Give the extent of all Plasmodium malariae-infected red blood cells.
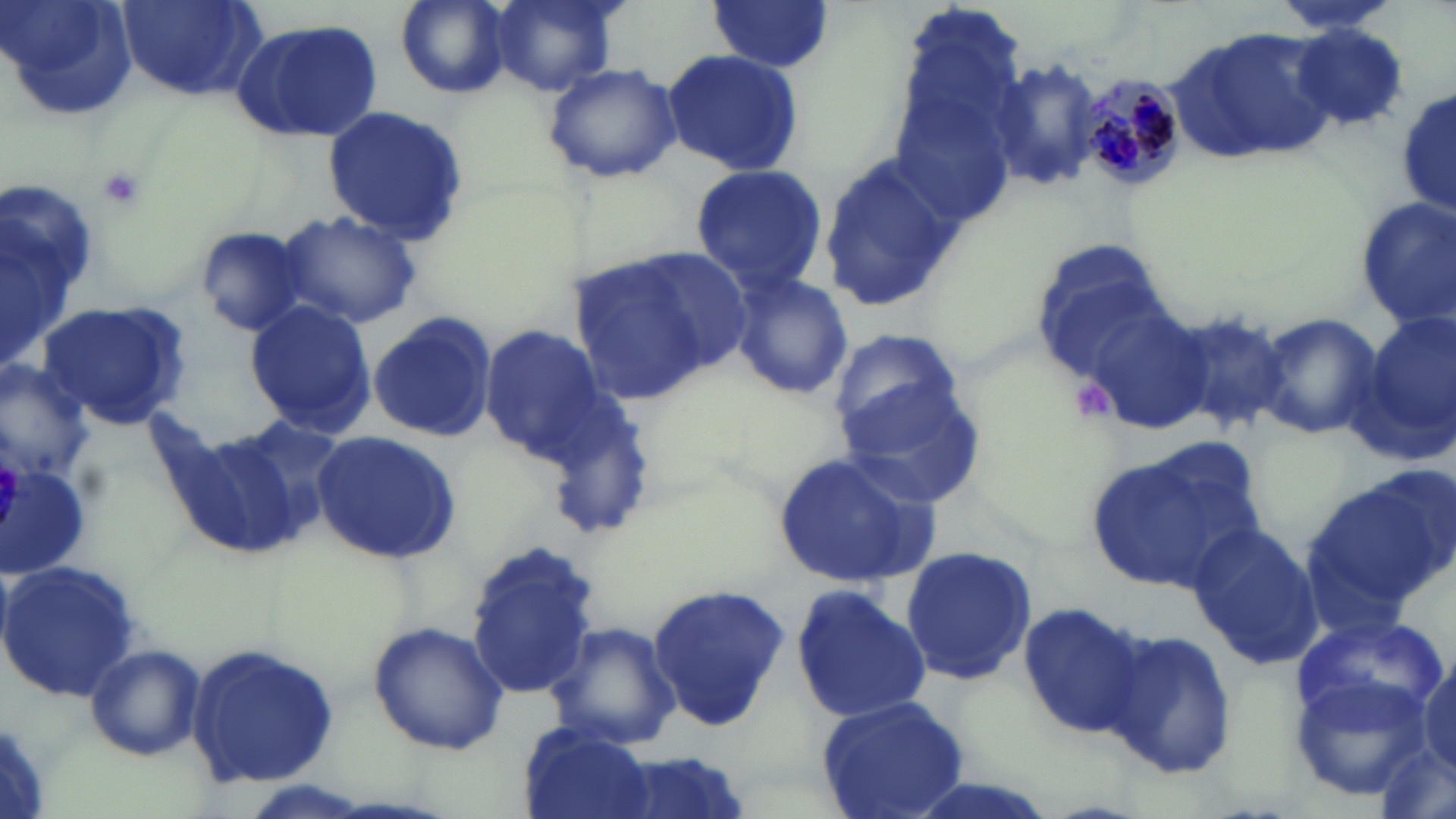

Approximate bounding boxes as named x1/y1/x2/y2 corners in pixels.
Plasmodium malariae-infected red blood cells: (x1=1078, y1=76, x2=1185, y2=193).

slide-level diagnosis = Plasmodium malariae
platelet locations = approximate bounding boxes as named x1/y1/x2/y2 corners in pixels: (x1=93, y1=166, x2=147, y2=210), (x1=1070, y1=381, x2=1116, y2=420)
uninfected red blood cell locations = approximate bounding boxes as named x1/y1/x2/y2 corners in pixels: (x1=1, y1=0, x2=138, y2=123), (x1=118, y1=0, x2=265, y2=103), (x1=394, y1=0, x2=511, y2=98), (x1=489, y1=0, x2=620, y2=95), (x1=705, y1=1, x2=837, y2=75), (x1=1271, y1=2, x2=1402, y2=35), (x1=231, y1=19, x2=382, y2=142), (x1=1292, y1=25, x2=1406, y2=128), (x1=886, y1=31, x2=1029, y2=229), (x1=1177, y1=31, x2=1340, y2=162), (x1=660, y1=48, x2=806, y2=175), (x1=542, y1=60, x2=682, y2=186), (x1=992, y1=61, x2=1102, y2=195), (x1=1399, y1=87, x2=1455, y2=220), (x1=320, y1=104, x2=470, y2=242), (x1=818, y1=152, x2=963, y2=312), (x1=689, y1=162, x2=827, y2=295), (x1=0, y1=183, x2=99, y2=373), (x1=1356, y1=194, x2=1455, y2=328), (x1=275, y1=208, x2=422, y2=329), (x1=192, y1=224, x2=314, y2=338), (x1=1030, y1=238, x2=1173, y2=381), (x1=565, y1=251, x2=729, y2=405), (x1=728, y1=272, x2=854, y2=402), (x1=37, y1=300, x2=192, y2=431), (x1=244, y1=301, x2=375, y2=435), (x1=1166, y1=304, x2=1289, y2=434), (x1=1084, y1=305, x2=1216, y2=435), (x1=367, y1=311, x2=498, y2=445), (x1=1256, y1=312, x2=1381, y2=440), (x1=1363, y1=314, x2=1455, y2=453), (x1=479, y1=323, x2=615, y2=463), (x1=828, y1=329, x2=970, y2=454), (x1=0, y1=358, x2=96, y2=484), (x1=841, y1=383, x2=989, y2=511), (x1=163, y1=413, x2=344, y2=563), (x1=311, y1=429, x2=459, y2=566), (x1=1088, y1=443, x2=1261, y2=592), (x1=772, y1=447, x2=940, y2=589), (x1=1, y1=461, x2=92, y2=578), (x1=1310, y1=467, x2=1451, y2=614), (x1=1187, y1=520, x2=1322, y2=670), (x1=466, y1=540, x2=600, y2=698), (x1=899, y1=545, x2=1036, y2=689), (x1=0, y1=559, x2=139, y2=700), (x1=791, y1=583, x2=932, y2=726), (x1=647, y1=584, x2=789, y2=730), (x1=1017, y1=599, x2=1145, y2=735), (x1=543, y1=620, x2=681, y2=751), (x1=369, y1=621, x2=509, y2=756), (x1=1102, y1=628, x2=1237, y2=779), (x1=83, y1=642, x2=207, y2=760), (x1=186, y1=642, x2=340, y2=790), (x1=1415, y1=650, x2=1456, y2=776), (x1=813, y1=695, x2=972, y2=819), (x1=517, y1=724, x2=655, y2=819), (x1=601, y1=752, x2=759, y2=819)
preparation = thin blood smear
modality = light microscopy
stain = May-Grünwald-Giemsa
field of view = single
image size = 1456×819 pixels
magnification = 1000x